State the blood parasite species.
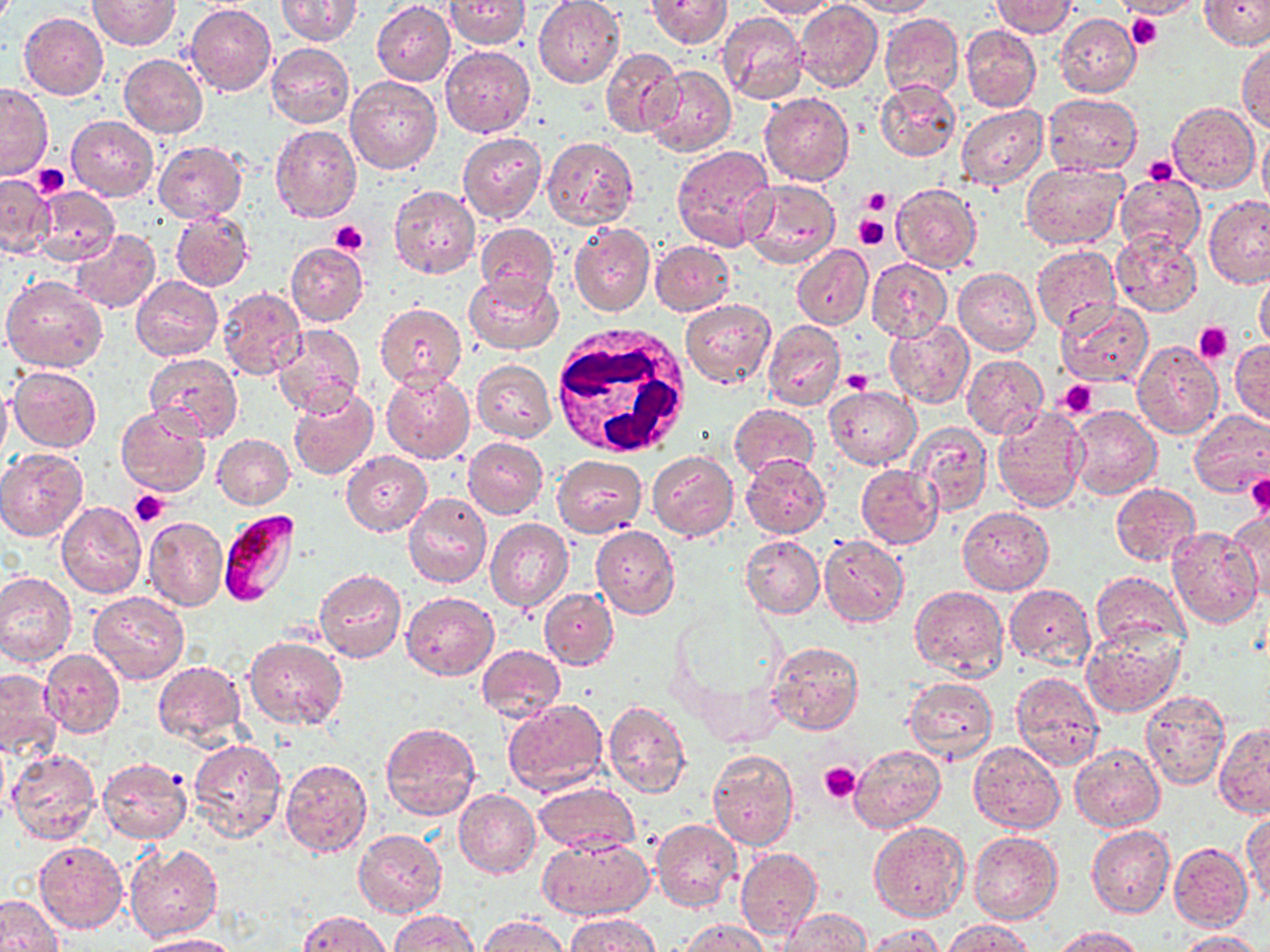
Plasmodium falciparum.

stain = May-Grünwald-Giemsa
image size = 1270×952 pixels
preparation = thin blood smear
Plasmodium falciparum-infected red blood cell locations = approximate bounding boxes as (x1, y1, x2, y2) in pixels: (217, 510, 299, 608)
modality = optical microscopy
field of view = one of a larger specimen
uninfected red blood cell locations = approximate bounding boxes as (x1, y1, x2, y2) in pixels: (276, 0, 361, 45), (444, 0, 530, 50), (647, 0, 730, 49), (752, 0, 837, 19), (847, 0, 938, 17), (1117, 0, 1201, 19), (1200, 0, 1270, 50), (88, 1, 180, 50), (533, 1, 624, 88), (794, 1, 882, 91), (990, 1, 1078, 37), (372, 2, 455, 85), (186, 4, 276, 96), (717, 11, 809, 105), (20, 13, 108, 99), (880, 13, 964, 99), (1056, 13, 1141, 97), (960, 24, 1042, 112), (1237, 41, 1270, 133), (266, 43, 355, 128), (441, 45, 534, 137), (600, 49, 682, 138), (119, 54, 207, 138), (645, 65, 736, 157), (345, 75, 441, 174), (874, 79, 960, 162), (0, 85, 51, 179), (759, 93, 854, 185), (1044, 93, 1142, 174), (1168, 103, 1259, 193), (957, 104, 1048, 190), (67, 116, 157, 200), (271, 125, 361, 222), (1257, 125, 1270, 214), (458, 133, 547, 224), (543, 136, 638, 229), (153, 141, 246, 222), (672, 144, 776, 251), (1020, 161, 1127, 249), (0, 173, 54, 257), (1115, 173, 1206, 255), (740, 178, 841, 269), (889, 183, 983, 272), (32, 185, 119, 265), (389, 185, 480, 278), (1204, 195, 1270, 288), (170, 209, 253, 291), (569, 221, 655, 316), (476, 223, 561, 301), (71, 228, 160, 314), (1110, 229, 1202, 317), (649, 241, 736, 316), (287, 242, 367, 326), (791, 244, 873, 330), (1032, 245, 1122, 334), (866, 258, 951, 341), (956, 259, 1121, 344), (952, 267, 1039, 356), (1255, 270, 1270, 354), (465, 272, 562, 354), (2, 275, 109, 373), (131, 275, 222, 360), (217, 286, 306, 379), (679, 298, 775, 390), (1055, 300, 1153, 387), (374, 302, 468, 388), (763, 318, 845, 411), (885, 318, 974, 408), (273, 323, 366, 418), (1132, 340, 1223, 439), (1229, 340, 1270, 425), (145, 353, 242, 442), (961, 354, 1048, 439), (471, 359, 556, 442), (8, 365, 101, 452), (381, 370, 475, 463), (0, 382, 12, 469), (826, 386, 920, 469), (289, 388, 378, 480), (116, 404, 211, 497), (729, 404, 818, 482), (991, 405, 1089, 510), (1069, 406, 1161, 499), (1188, 409, 1270, 497), (908, 422, 992, 515), (213, 434, 294, 510), (463, 438, 547, 518), (0, 448, 88, 540), (342, 451, 431, 536), (648, 451, 738, 540), (741, 453, 832, 539), (552, 455, 646, 537), (856, 465, 943, 548), (1111, 483, 1200, 566), (404, 491, 491, 588), (57, 501, 146, 598), (957, 506, 1054, 594), (1224, 508, 1269, 604), (142, 517, 227, 611), (485, 518, 574, 612), (591, 525, 679, 619), (1168, 525, 1262, 627), (741, 534, 825, 617), (819, 534, 909, 627), (314, 569, 406, 662), (0, 570, 77, 665), (1090, 572, 1190, 651), (1004, 584, 1096, 669), (910, 585, 1008, 679), (540, 588, 618, 669), (88, 590, 189, 684), (402, 592, 498, 679), (1082, 624, 1185, 718), (244, 636, 347, 730), (769, 641, 864, 735), (477, 644, 565, 721), (40, 648, 124, 738), (153, 660, 246, 747), (0, 669, 63, 757), (1011, 671, 1104, 769), (903, 675, 996, 763), (1141, 689, 1230, 790), (503, 699, 608, 798), (603, 700, 690, 799), (380, 722, 483, 823), (1214, 724, 1270, 816), (189, 737, 286, 841), (968, 741, 1064, 834), (849, 744, 946, 833), (1071, 744, 1164, 832), (708, 749, 798, 850), (8, 750, 101, 846), (280, 757, 372, 857), (97, 758, 191, 844), (533, 782, 638, 855), (454, 788, 540, 878), (1243, 813, 1270, 909), (651, 819, 742, 912), (869, 821, 970, 921), (1088, 824, 1175, 918), (354, 830, 446, 917), (969, 831, 1062, 924), (537, 835, 653, 921), (34, 841, 127, 933), (126, 842, 222, 942), (1169, 842, 1252, 931), (736, 847, 823, 939), (0, 895, 62, 952), (779, 907, 871, 951), (390, 910, 479, 951), (297, 911, 394, 952), (563, 913, 662, 952), (478, 914, 570, 951), (680, 918, 770, 952), (942, 919, 1033, 952), (863, 924, 944, 952), (1055, 926, 1146, 952), (1173, 929, 1262, 951), (139, 934, 244, 952)
platelet locations = approximate bounding boxes as (x1, y1, x2, y2) in pixels: (1128, 12, 1161, 51), (1144, 155, 1179, 185), (31, 162, 69, 197), (861, 188, 892, 215), (853, 214, 889, 250), (330, 220, 368, 256), (1194, 323, 1233, 364), (843, 370, 874, 396), (1057, 380, 1098, 418), (1245, 474, 1270, 517), (130, 489, 168, 527), (821, 763, 861, 803)
white blood cell locations = approximate bounding boxes as (x1, y1, x2, y2) in pixels: (553, 320, 695, 458)
magnification = 1000x